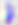

Summary:
  - Magnification: 400x
  - Identification: Toxoplasma gondii
  - Modality: micrograph